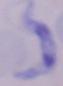

Summary:
  - Identification: trypanosome
  - Magnification: 1000x
  - Modality: micrograph